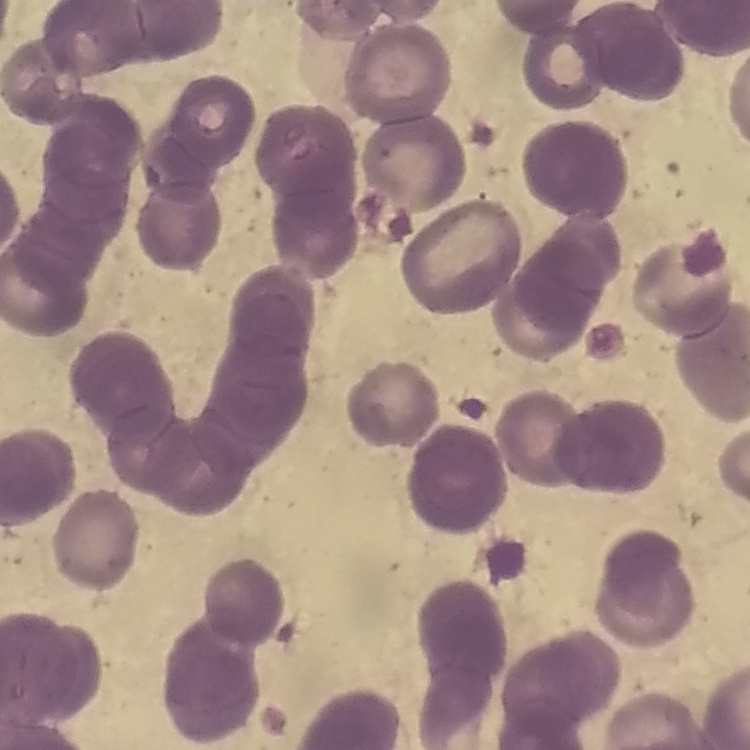

The red blood cells exhibit rouleaux formation. One tile cut from a larger photomicrograph. Thin blood smear. Field's or Giemsa stain.